Give the extent of all Plasmodium ovale-infected red blood cells.
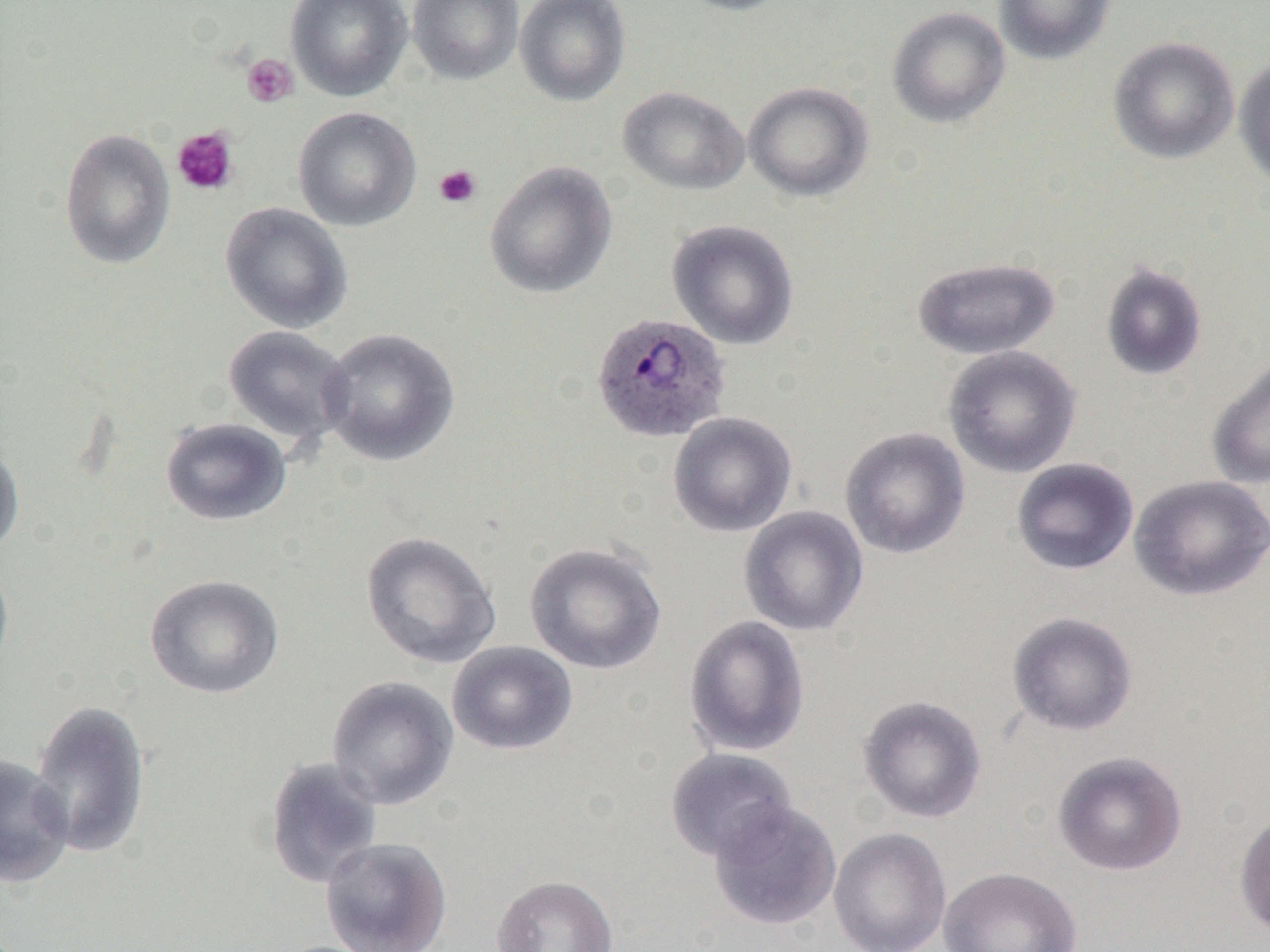
Approximate bounding boxes as (x1,y1)-(x2,y2) corner pairs in pixels.
Plasmodium ovale-infected red blood cells: (590,312)-(732,444).

Platelet locations: (241,54)-(299,108), (172,127)-(239,196), (434,164)-(481,209). Uninfected red blood cell locations: (285,0)-(412,102), (407,0)-(524,84), (514,0)-(631,106), (670,0)-(796,16), (994,0)-(1116,65), (887,6)-(1011,128), (1107,36)-(1240,164), (1233,54)-(1270,192), (743,81)-(873,201), (618,86)-(750,195), (292,106)-(421,232), (59,128)-(176,269), (484,161)-(618,299), (220,202)-(353,333), (667,219)-(799,350), (912,256)-(1061,359), (1100,261)-(1208,381), (223,325)-(355,446), (319,327)-(460,466), (942,345)-(1082,478), (1206,355)-(1270,490), (668,411)-(797,538), (160,417)-(291,526), (840,427)-(970,559), (0,438)-(25,561), (1011,458)-(1139,576), (1129,474)-(1270,601), (739,506)-(869,637), (361,530)-(501,670), (524,541)-(667,674), (0,554)-(15,685), (144,574)-(285,699), (1006,611)-(1138,736), (683,615)-(811,757), (447,640)-(578,756), (326,675)-(459,810), (857,694)-(987,823), (28,698)-(151,860), (665,748)-(799,863), (1052,751)-(1187,876), (0,754)-(74,888), (264,756)-(384,889), (708,800)-(841,930), (1234,808)-(1270,940), (829,827)-(952,952), (321,837)-(453,952), (939,866)-(1082,952), (491,874)-(618,952). Slide-level diagnosis: Plasmodium ovale. Captured at 1000x magnification. One field of a larger specimen. Image is 1270×952 pixels. Thin blood film. Optical microscopy.